Assess this cell for malaria.
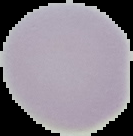
Uninfected.

Summary:
  - Image size: 133×136 pixels
  - Image type: segmented cell region with the area outside set to black
  - Preparation: thin blood smear